Name the parasite shown.
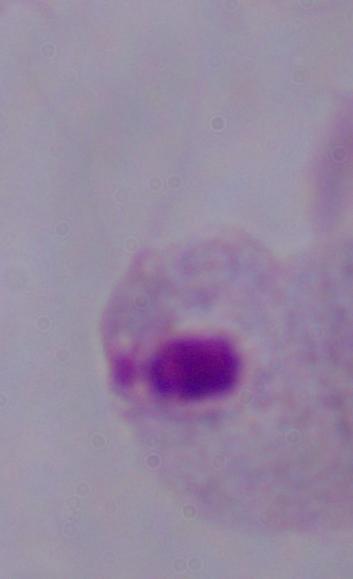
A trichomonad.

magnification = 1000x
modality = photomicrograph